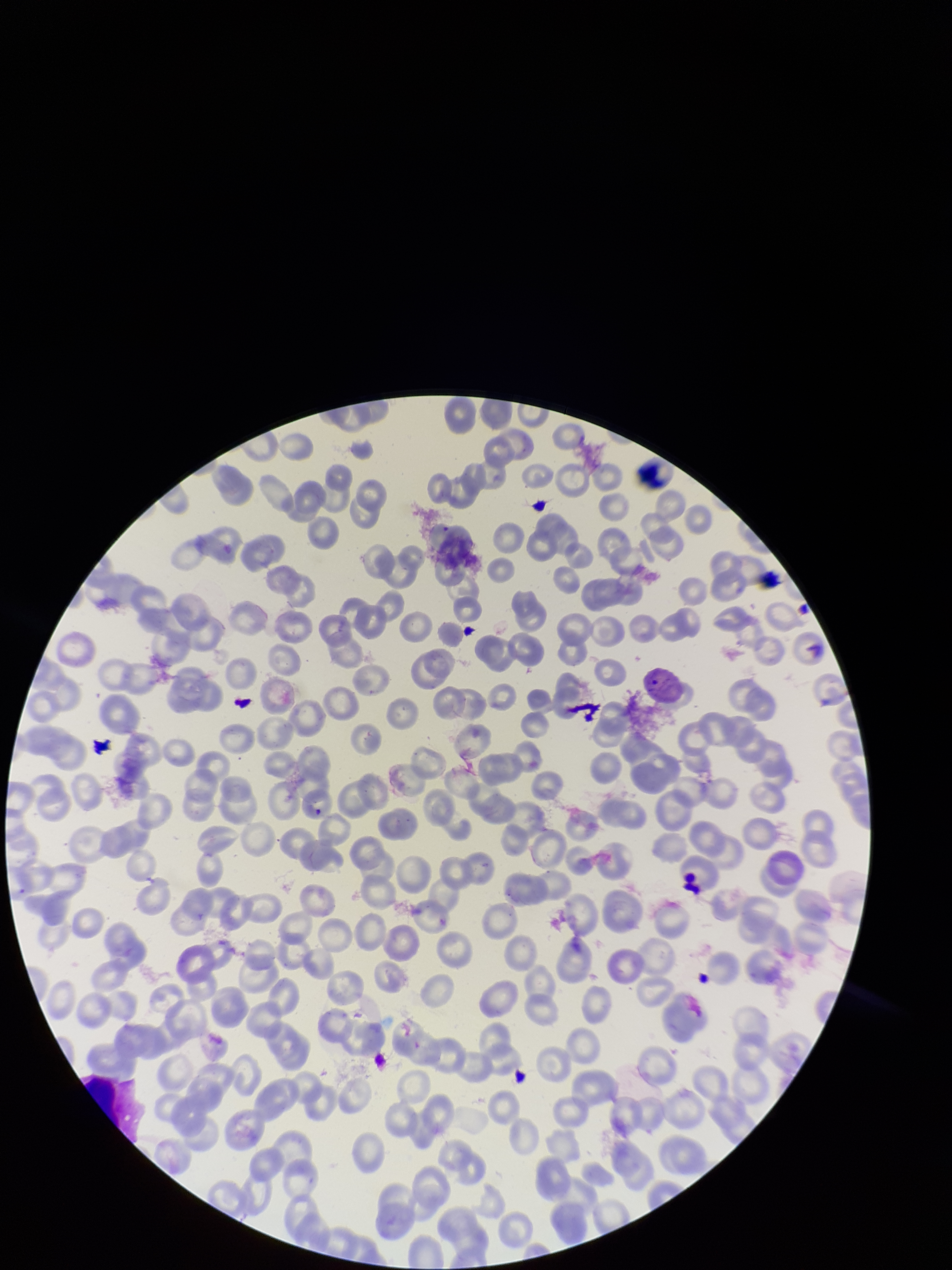

Patient malaria status: infected. Parasitized red blood cells: detected. Photographed through the microscope eyepiece with a smartphone camera. One field from this slide. Species reported for this patient: Plasmodium vivax. Image is 952×1270 pixels. Stained with Giemsa. Preparation: thin smear. Parasitized red blood cell count: 1. Red blood cell count: 180.